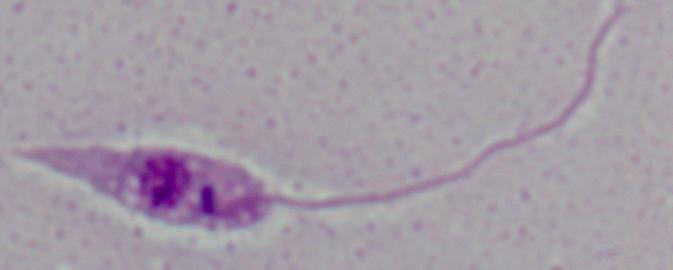

A Leishmania parasite is seen. 1000x magnification. Photomicrograph.